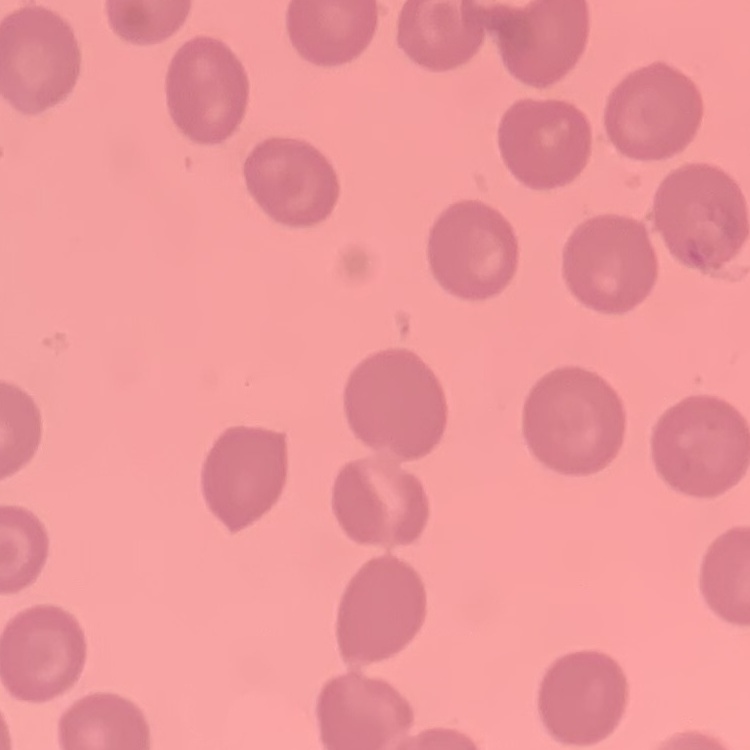

Summary:
  - Red blood cell morphology: no rouleaux formation
  - Preparation: thin blood film
  - Stain: Field's or Giemsa
  - Image type: one tile cut from a larger photomicrograph